Mark where platelets are.
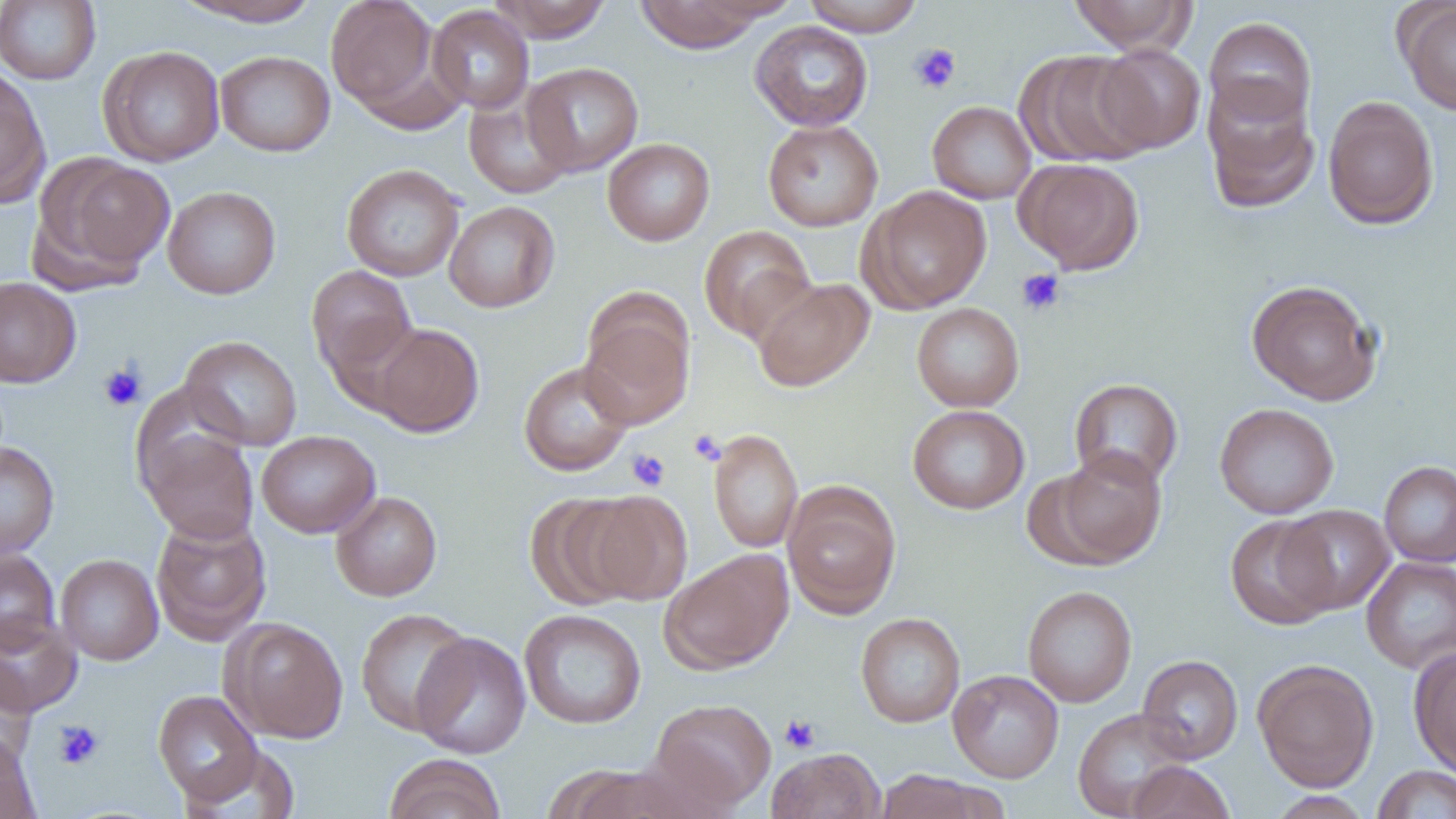

Approximate bounding boxes as named x1/y1/x2/y2 corners in pixels.
Platelets: (x1=909, y1=43, x2=962, y2=94), (x1=1016, y1=268, x2=1066, y2=316), (x1=98, y1=364, x2=146, y2=412), (x1=689, y1=430, x2=726, y2=465), (x1=627, y1=449, x2=670, y2=491), (x1=779, y1=713, x2=821, y2=753), (x1=53, y1=720, x2=104, y2=769).

Summary:
  - Uninfected red blood cell locations: (x1=172, y1=0, x2=324, y2=28), (x1=326, y1=0, x2=441, y2=117), (x1=489, y1=0, x2=612, y2=42), (x1=632, y1=0, x2=772, y2=53), (x1=802, y1=0, x2=924, y2=36), (x1=1067, y1=0, x2=1197, y2=54), (x1=0, y1=1, x2=101, y2=85), (x1=1397, y1=2, x2=1456, y2=115), (x1=427, y1=5, x2=535, y2=113), (x1=1204, y1=16, x2=1317, y2=128), (x1=749, y1=20, x2=874, y2=132), (x1=1093, y1=44, x2=1205, y2=154), (x1=98, y1=45, x2=225, y2=167), (x1=215, y1=50, x2=335, y2=157), (x1=1017, y1=50, x2=1154, y2=168), (x1=522, y1=62, x2=644, y2=176), (x1=0, y1=66, x2=50, y2=207), (x1=1202, y1=80, x2=1320, y2=214), (x1=463, y1=88, x2=576, y2=200), (x1=1322, y1=95, x2=1439, y2=230), (x1=927, y1=100, x2=1036, y2=204), (x1=762, y1=119, x2=883, y2=231), (x1=602, y1=138, x2=715, y2=246), (x1=33, y1=156, x2=175, y2=286), (x1=1015, y1=158, x2=1144, y2=275), (x1=341, y1=163, x2=465, y2=282), (x1=859, y1=185, x2=993, y2=314), (x1=162, y1=186, x2=281, y2=299), (x1=443, y1=200, x2=560, y2=313), (x1=698, y1=225, x2=816, y2=342), (x1=305, y1=264, x2=416, y2=379), (x1=0, y1=276, x2=82, y2=388), (x1=752, y1=277, x2=875, y2=391), (x1=1245, y1=279, x2=1383, y2=405), (x1=579, y1=297, x2=695, y2=430), (x1=911, y1=302, x2=1024, y2=412), (x1=368, y1=322, x2=484, y2=437), (x1=178, y1=335, x2=303, y2=451), (x1=518, y1=361, x2=633, y2=476), (x1=1069, y1=378, x2=1183, y2=487), (x1=131, y1=381, x2=250, y2=498), (x1=1214, y1=402, x2=1339, y2=519), (x1=907, y1=404, x2=1030, y2=514), (x1=709, y1=428, x2=803, y2=553), (x1=141, y1=430, x2=259, y2=543), (x1=256, y1=430, x2=380, y2=538), (x1=0, y1=441, x2=59, y2=560), (x1=1047, y1=449, x2=1169, y2=568), (x1=1379, y1=461, x2=1456, y2=567), (x1=783, y1=484, x2=901, y2=618), (x1=576, y1=490, x2=693, y2=605), (x1=331, y1=491, x2=442, y2=601), (x1=526, y1=492, x2=646, y2=611), (x1=1277, y1=504, x2=1395, y2=614), (x1=150, y1=514, x2=271, y2=645), (x1=1224, y1=515, x2=1340, y2=630), (x1=0, y1=548, x2=60, y2=654), (x1=660, y1=550, x2=794, y2=674), (x1=55, y1=554, x2=164, y2=665), (x1=1361, y1=556, x2=1456, y2=674), (x1=1022, y1=585, x2=1138, y2=707), (x1=355, y1=606, x2=474, y2=735), (x1=519, y1=608, x2=647, y2=729), (x1=0, y1=612, x2=82, y2=718), (x1=855, y1=612, x2=965, y2=728), (x1=222, y1=617, x2=348, y2=743), (x1=411, y1=631, x2=532, y2=759), (x1=1409, y1=647, x2=1456, y2=778), (x1=1137, y1=654, x2=1243, y2=764), (x1=1253, y1=659, x2=1379, y2=791), (x1=0, y1=661, x2=37, y2=768), (x1=947, y1=669, x2=1064, y2=783), (x1=152, y1=689, x2=263, y2=808), (x1=647, y1=697, x2=777, y2=812), (x1=1072, y1=708, x2=1195, y2=819), (x1=0, y1=732, x2=40, y2=819), (x1=766, y1=747, x2=886, y2=819), (x1=383, y1=754, x2=506, y2=819), (x1=1126, y1=760, x2=1235, y2=819), (x1=552, y1=764, x2=698, y2=818), (x1=1371, y1=765, x2=1456, y2=818), (x1=873, y1=768, x2=1006, y2=819), (x1=1268, y1=790, x2=1373, y2=819)
  - Slide-level diagnosis: negative for blood parasites
  - Preparation: thin blood smear
  - Field of view: single
  - Magnification: 1000x
  - Modality: light microscopy
  - Image size: 1456×819 pixels